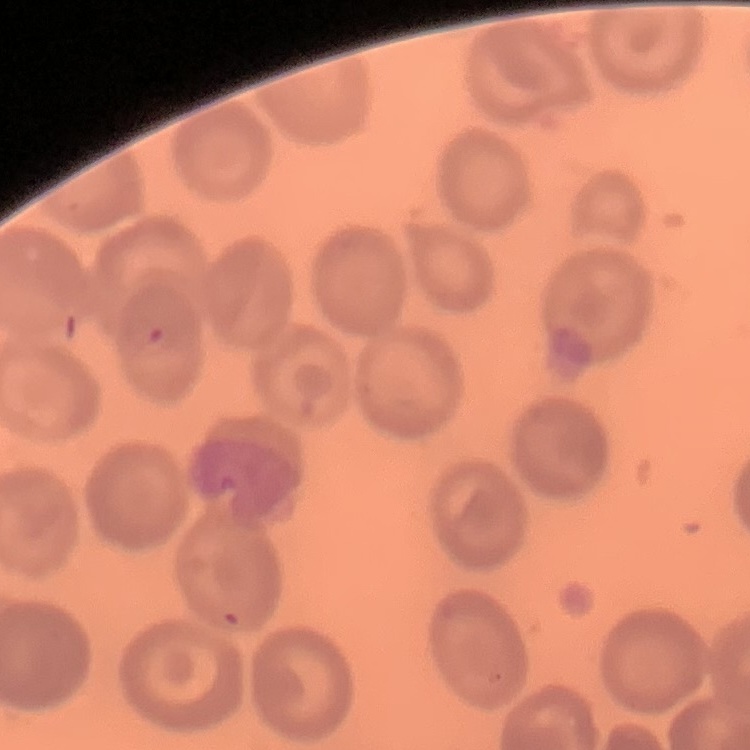

Summary:
  - Red blood cell morphology: no rouleaux formation
  - Stain: Field's or Giemsa
  - Image type: one tile cut from a larger photomicrograph
  - Preparation: thin peripheral smear